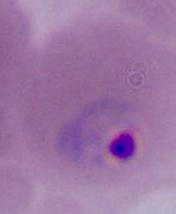

magnification = 400x or 1000x
identification = Plasmodium
modality = photomicrograph